Name the cell type shown.
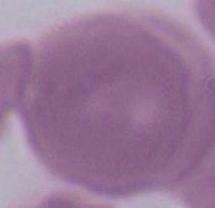
This is an erythrocyte.

Summary:
  - Magnification: 1000x
  - Modality: photomicrograph